Point out each Plasmodium parasite.
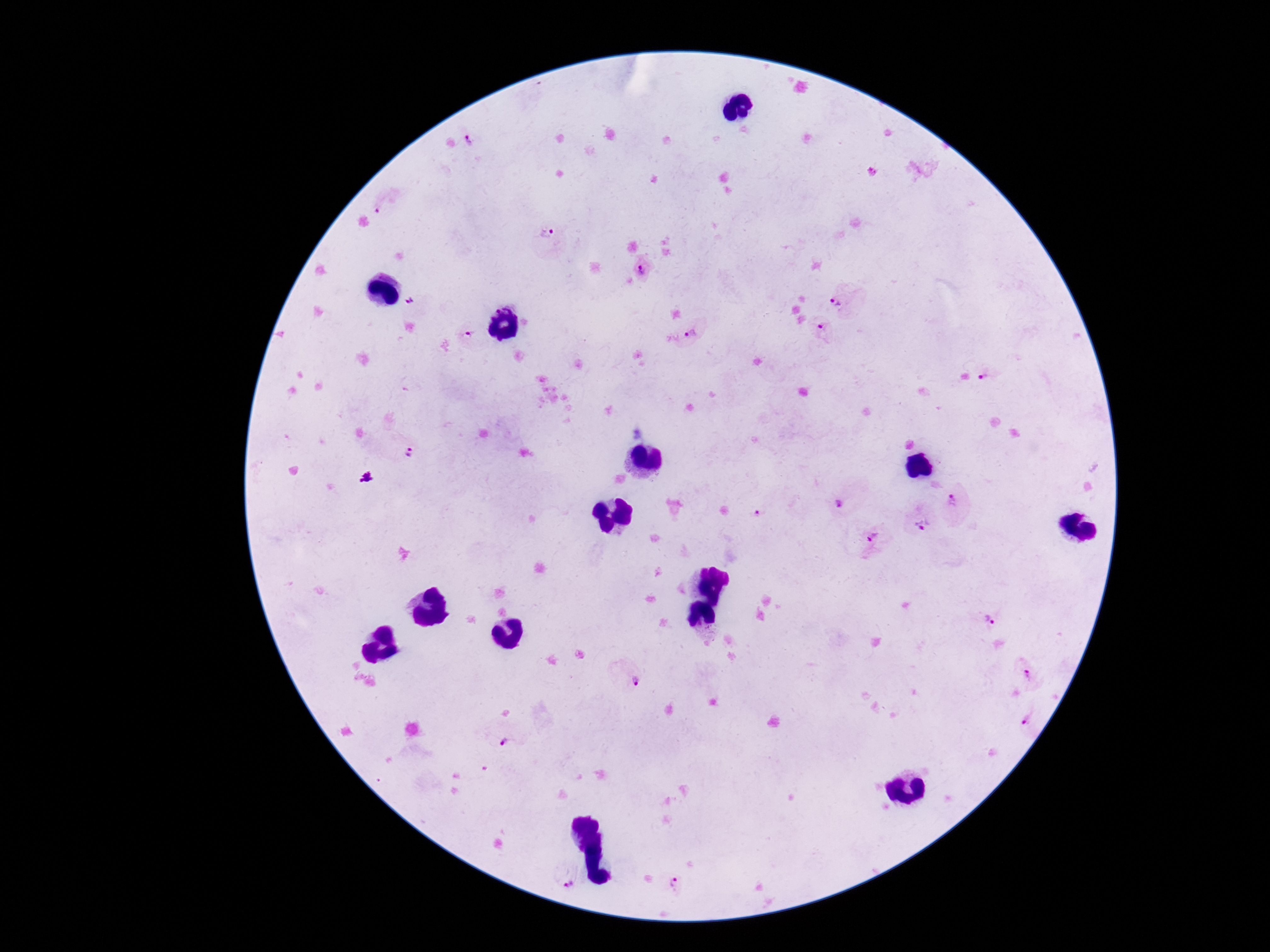

Approximate object centers, in pixels from the top-left corner.
Plasmodium parasites: (x=468, y=141), (x=381, y=205), (x=544, y=230), (x=642, y=267), (x=410, y=299), (x=845, y=300), (x=821, y=331), (x=694, y=332), (x=469, y=333), (x=989, y=375), (x=408, y=451), (x=366, y=477), (x=837, y=499), (x=960, y=504), (x=758, y=513), (x=920, y=524), (x=870, y=543), (x=989, y=617), (x=627, y=674), (x=1026, y=675), (x=1032, y=721), (x=505, y=737), (x=566, y=873), (x=678, y=887).

capture = smartphone camera through the microscope eyepiece
preparation = thick blood smear
field of view = single
image size = 1270×952 pixels
magnification = 100x
patient malaria status = infected
stain = Giemsa